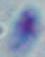
Summary:
  - Identification: Toxoplasma gondii
  - Magnification: 1000x
  - Modality: photomicrograph